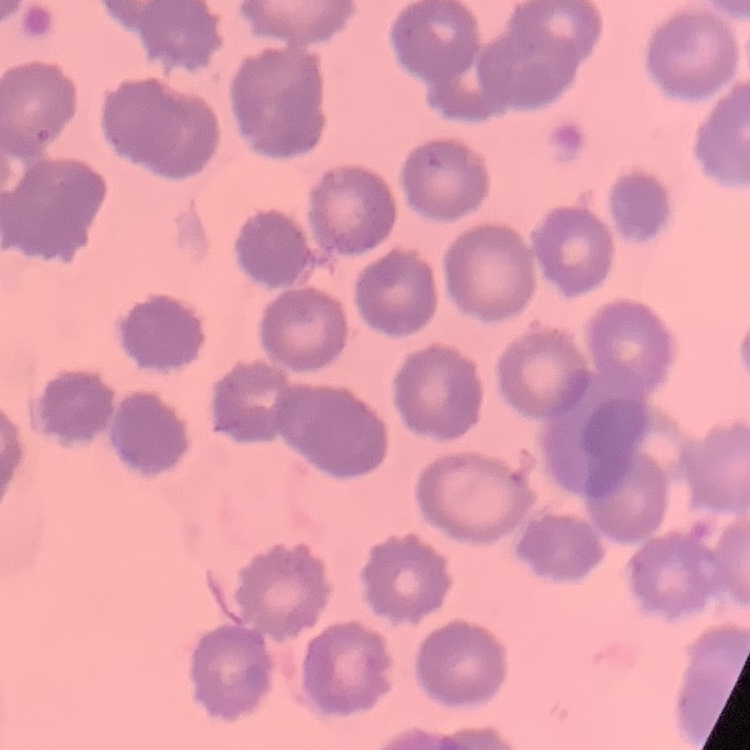

red_blood_cell_morphology: no rouleaux formation
stain: Field's or Giemsa
image_type: one tile cut from a larger photomicrograph
preparation: thin blood smear